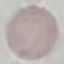

Summary:
  - Result: negative for malaria parasites
  - Stain: Giemsa
  - Image type: automatically extracted cell patch, resized to 64 × 64 pixels
  - Preparation: thin blood film
  - Capture: smartphone through the microscope eyepiece